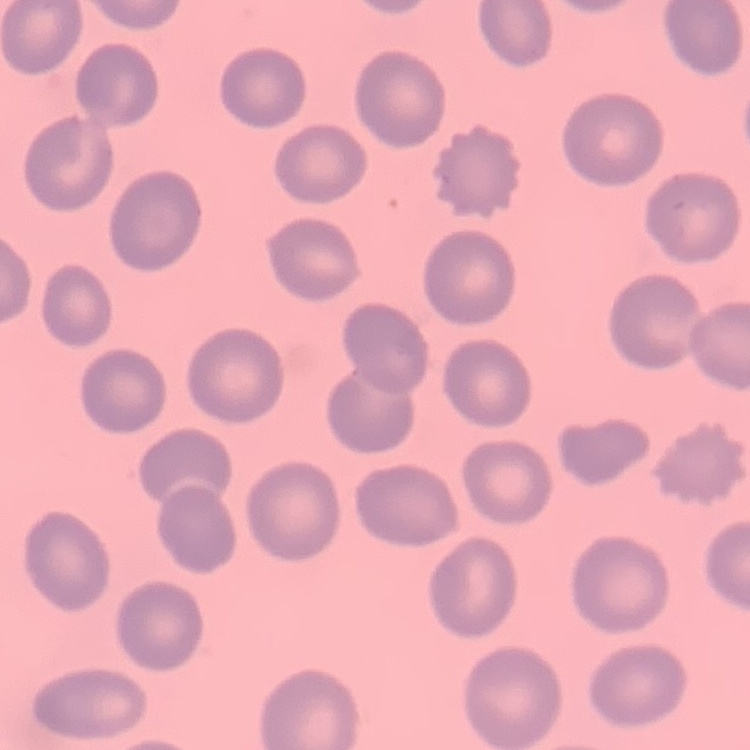
Summary:
  - Erythrocyte morphology: no rouleaux formation
  - Stain: Field's or Giemsa
  - Preparation: thin blood film
  - Image type: one tile cut from a larger photomicrograph